Identify the blood parasite species.
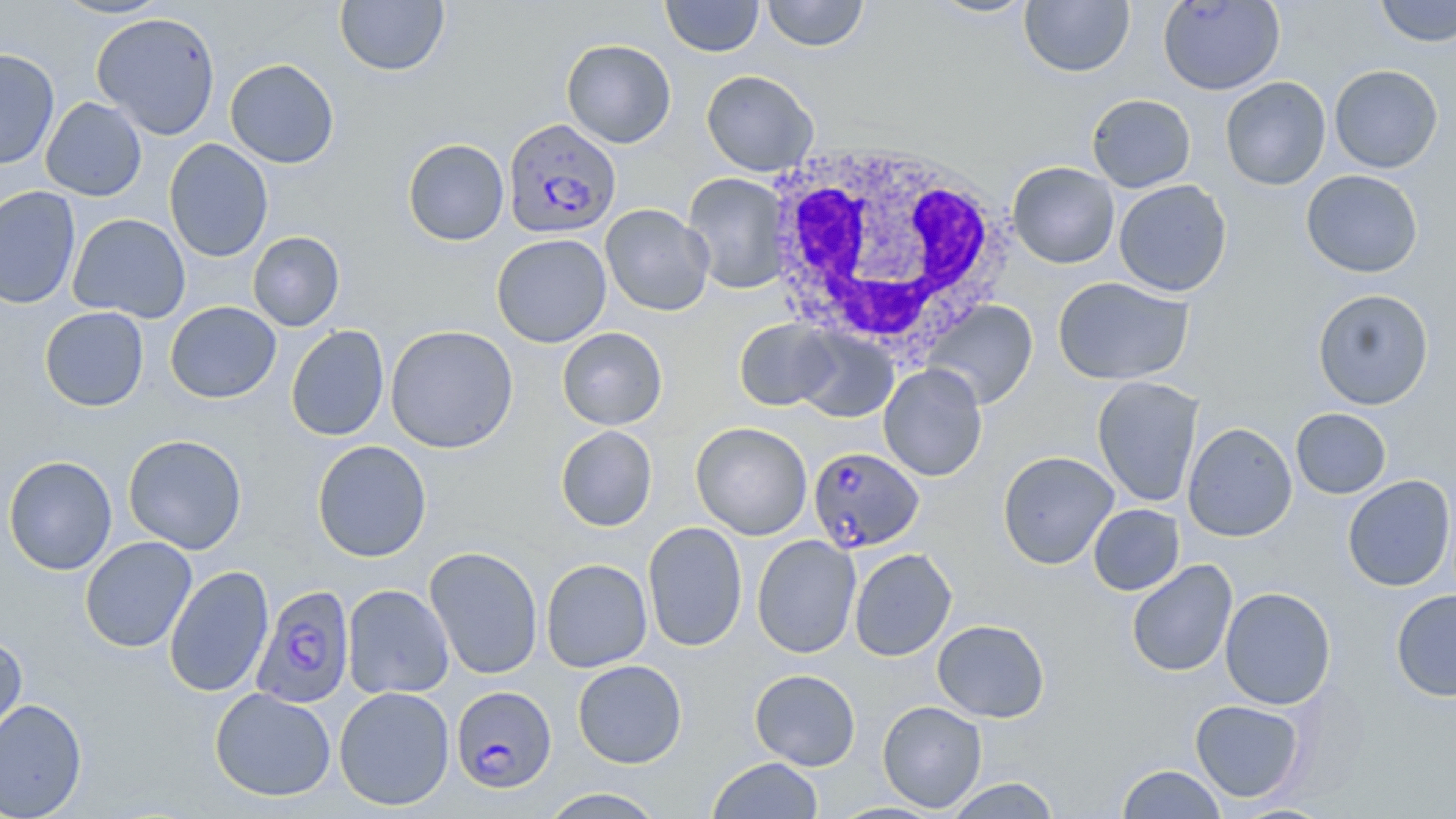

Plasmodium falciparum.

Summary:
  - Coordinate format: approximate bounding boxes as named x1/y1/x2/y2 corners in pixels
  - White blood cell locations: (x1=764, y1=140, x2=1013, y2=355)
  - Uninfected red blood cell locations: (x1=52, y1=0, x2=173, y2=19), (x1=660, y1=0, x2=764, y2=57), (x1=761, y1=0, x2=869, y2=51), (x1=924, y1=0, x2=1040, y2=19), (x1=1019, y1=0, x2=1135, y2=77), (x1=1157, y1=0, x2=1285, y2=95), (x1=1375, y1=0, x2=1456, y2=47), (x1=334, y1=1, x2=449, y2=76), (x1=91, y1=11, x2=221, y2=140), (x1=561, y1=39, x2=676, y2=148), (x1=0, y1=48, x2=59, y2=170), (x1=225, y1=58, x2=340, y2=169), (x1=1329, y1=64, x2=1443, y2=173), (x1=701, y1=70, x2=819, y2=176), (x1=1220, y1=76, x2=1331, y2=190), (x1=1086, y1=94, x2=1196, y2=193), (x1=40, y1=97, x2=147, y2=201), (x1=402, y1=138, x2=509, y2=246), (x1=164, y1=139, x2=274, y2=262), (x1=1007, y1=162, x2=1120, y2=268), (x1=1301, y1=169, x2=1423, y2=278), (x1=682, y1=173, x2=790, y2=293), (x1=1114, y1=179, x2=1232, y2=297), (x1=0, y1=185, x2=81, y2=310), (x1=600, y1=203, x2=714, y2=316), (x1=67, y1=213, x2=191, y2=322), (x1=247, y1=231, x2=345, y2=332), (x1=491, y1=233, x2=612, y2=347), (x1=1053, y1=276, x2=1194, y2=386), (x1=1312, y1=288, x2=1435, y2=409), (x1=922, y1=300, x2=1038, y2=409), (x1=165, y1=301, x2=281, y2=403), (x1=39, y1=306, x2=149, y2=412), (x1=733, y1=319, x2=840, y2=411), (x1=286, y1=325, x2=389, y2=442), (x1=385, y1=325, x2=518, y2=454), (x1=557, y1=327, x2=667, y2=430), (x1=792, y1=328, x2=898, y2=422), (x1=878, y1=363, x2=988, y2=481), (x1=1092, y1=376, x2=1204, y2=507), (x1=1291, y1=408, x2=1392, y2=499), (x1=690, y1=422, x2=813, y2=540), (x1=1182, y1=422, x2=1297, y2=542), (x1=555, y1=425, x2=658, y2=532), (x1=123, y1=434, x2=248, y2=554), (x1=311, y1=440, x2=432, y2=563), (x1=997, y1=450, x2=1119, y2=569), (x1=3, y1=455, x2=118, y2=575), (x1=1342, y1=475, x2=1455, y2=592), (x1=1088, y1=504, x2=1185, y2=595), (x1=642, y1=521, x2=748, y2=652), (x1=751, y1=535, x2=861, y2=658), (x1=80, y1=536, x2=197, y2=653), (x1=424, y1=546, x2=543, y2=679), (x1=849, y1=548, x2=957, y2=661), (x1=541, y1=558, x2=652, y2=672), (x1=1126, y1=559, x2=1238, y2=677), (x1=164, y1=565, x2=274, y2=698), (x1=342, y1=584, x2=454, y2=699), (x1=1219, y1=586, x2=1336, y2=709), (x1=1391, y1=589, x2=1456, y2=701), (x1=932, y1=619, x2=1050, y2=723), (x1=0, y1=633, x2=27, y2=749), (x1=572, y1=659, x2=687, y2=768), (x1=749, y1=668, x2=861, y2=770), (x1=334, y1=686, x2=455, y2=810), (x1=210, y1=687, x2=336, y2=802), (x1=0, y1=697, x2=87, y2=819), (x1=1190, y1=699, x2=1306, y2=803), (x1=877, y1=700, x2=987, y2=812), (x1=707, y1=757, x2=824, y2=818), (x1=1116, y1=764, x2=1228, y2=818), (x1=945, y1=777, x2=1061, y2=818), (x1=539, y1=788, x2=667, y2=818), (x1=1229, y1=802, x2=1337, y2=818)
  - Plasmodium falciparum-infected red blood cell locations: (x1=503, y1=117, x2=621, y2=239), (x1=808, y1=446, x2=924, y2=553), (x1=251, y1=584, x2=354, y2=709), (x1=450, y1=687, x2=556, y2=794)
  - Stain: May-Grünwald-Giemsa
  - Modality: light microscopy
  - Field of view: single
  - Image size: 1456×819 pixels
  - Preparation: thin blood smear
  - Magnification: 1000x